Assess this cell for malaria.
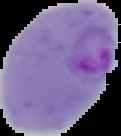
It is parasitized.

From a thin blood film. The area outside the segmented cell region is set to black. Image is 121×136 pixels.